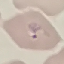

Result: malaria parasites detected. Thin blood smear. Acquired by smartphone through the microscope eyepiece. Automatically extracted cell patch, resized to 64 × 64 pixels. Giemsa stain.